Outline each blood parasite and name the species.
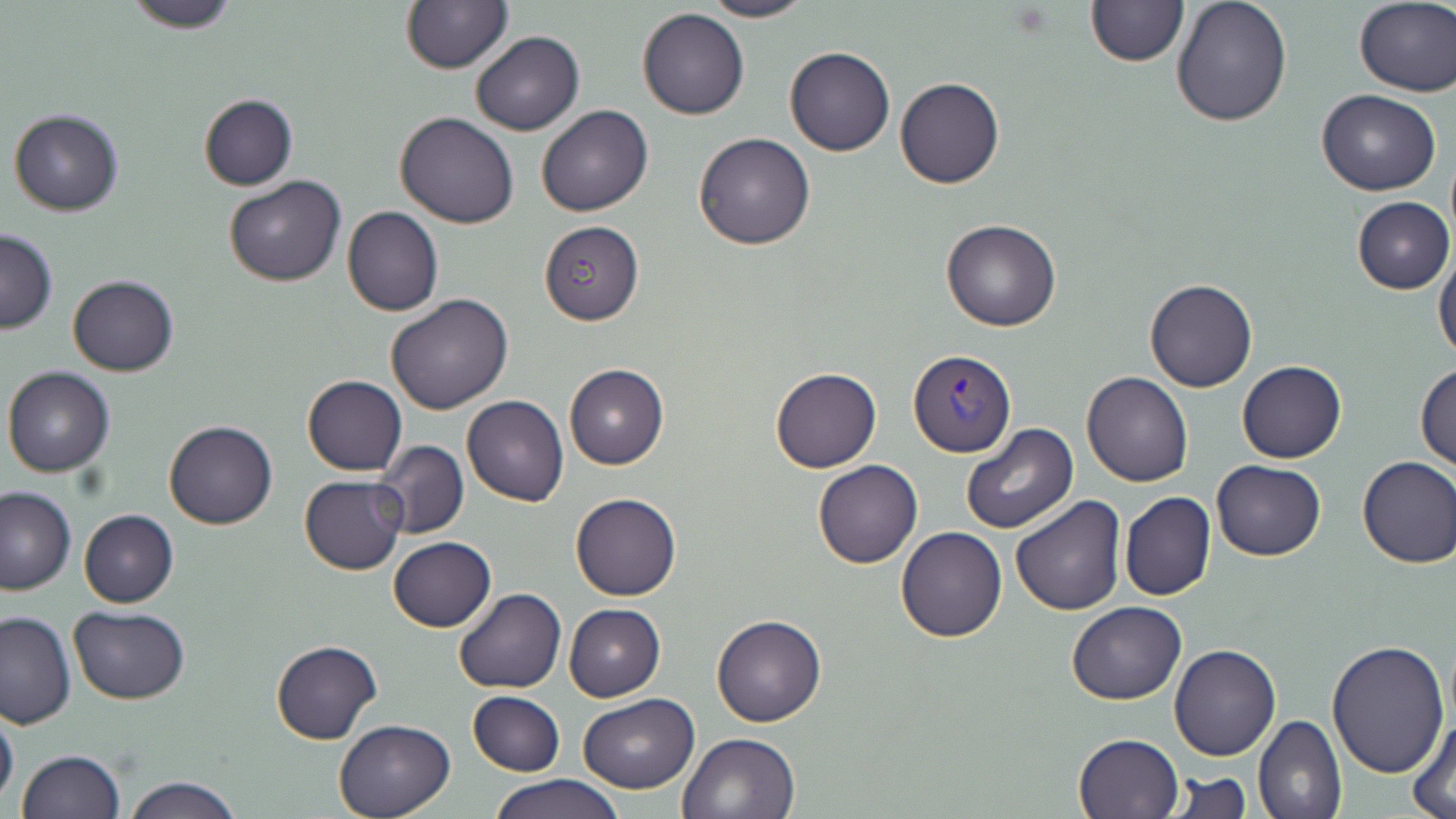

Approximate bounding boxes as [x1, y1, x2, y2] in pixels.
Plasmodium vivax-infected red blood cells: [907, 349, 1015, 456].
No Plasmodium falciparum, Plasmodium ovale, Plasmodium malariae, Babesia divergens, or Trypanosoma brucei observed.

Summary:
  - Uninfected red blood cell locations: [119, 0, 246, 33], [699, 0, 816, 23], [1171, 0, 1292, 125], [400, 1, 512, 73], [1084, 1, 1188, 68], [1354, 1, 1455, 96], [636, 7, 749, 120], [471, 31, 584, 134], [784, 46, 894, 156], [895, 77, 1005, 188], [1317, 90, 1442, 195], [198, 94, 299, 191], [535, 104, 653, 217], [8, 107, 124, 217], [394, 110, 520, 229], [693, 132, 815, 249], [224, 176, 346, 287], [1352, 196, 1454, 294], [342, 206, 443, 317], [941, 219, 1062, 331], [539, 220, 644, 325], [0, 229, 57, 333], [1434, 250, 1456, 365], [67, 275, 179, 376], [1145, 278, 1259, 393], [385, 294, 513, 414], [1238, 360, 1346, 463], [564, 363, 667, 469], [1415, 364, 1456, 471], [2, 366, 116, 477], [770, 366, 881, 473], [1082, 372, 1192, 488], [301, 374, 407, 476], [462, 396, 568, 507], [165, 421, 278, 530], [961, 423, 1077, 534], [374, 439, 468, 538], [1356, 455, 1456, 568], [812, 459, 923, 569], [1211, 460, 1325, 561], [300, 475, 408, 574], [0, 485, 75, 594], [1120, 492, 1216, 601], [570, 493, 681, 601], [1008, 496, 1126, 616], [78, 509, 179, 607], [896, 527, 1007, 642], [388, 537, 495, 632], [453, 588, 565, 694], [1065, 602, 1186, 705], [565, 604, 665, 702], [68, 606, 192, 704], [0, 609, 75, 728], [712, 612, 827, 728], [1326, 638, 1451, 778], [271, 640, 381, 745], [1169, 644, 1280, 762], [467, 690, 565, 775], [578, 694, 701, 793], [0, 702, 19, 809], [1408, 711, 1456, 818], [1253, 714, 1346, 819], [333, 718, 456, 818], [677, 731, 801, 819], [1073, 733, 1182, 818], [14, 750, 125, 819], [1163, 770, 1252, 819], [490, 773, 625, 819], [121, 776, 244, 819]
  - Slide-level diagnosis: Plasmodium vivax
  - Field of view: one of a larger specimen
  - Stain: May-Grünwald-Giemsa
  - Magnification: 1000x
  - Modality: optical microscopy
  - Preparation: thin blood film
  - Image size: 1456×819 pixels